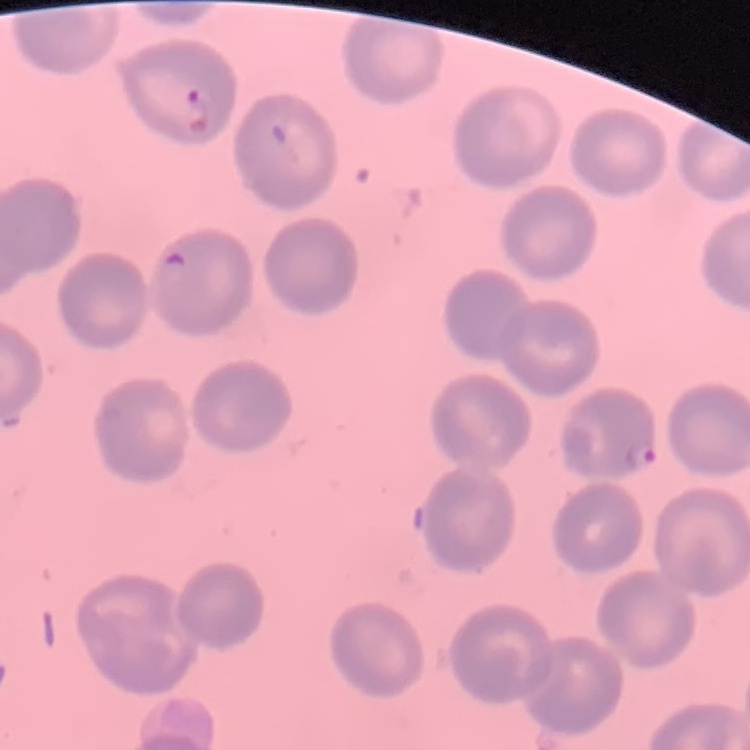
red blood cell morphology = no rouleaux formation
preparation = thin peripheral smear
image type = one tile cut from a larger photomicrograph
stain = Field's or Giemsa